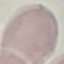
Summary:
  - Malaria status: uninfected
  - Capture: smartphone through the microscope eyepiece
  - Preparation: thin blood smear
  - Stain: Giemsa
  - Image type: automatically extracted cell patch, resized to 64 × 64 pixels